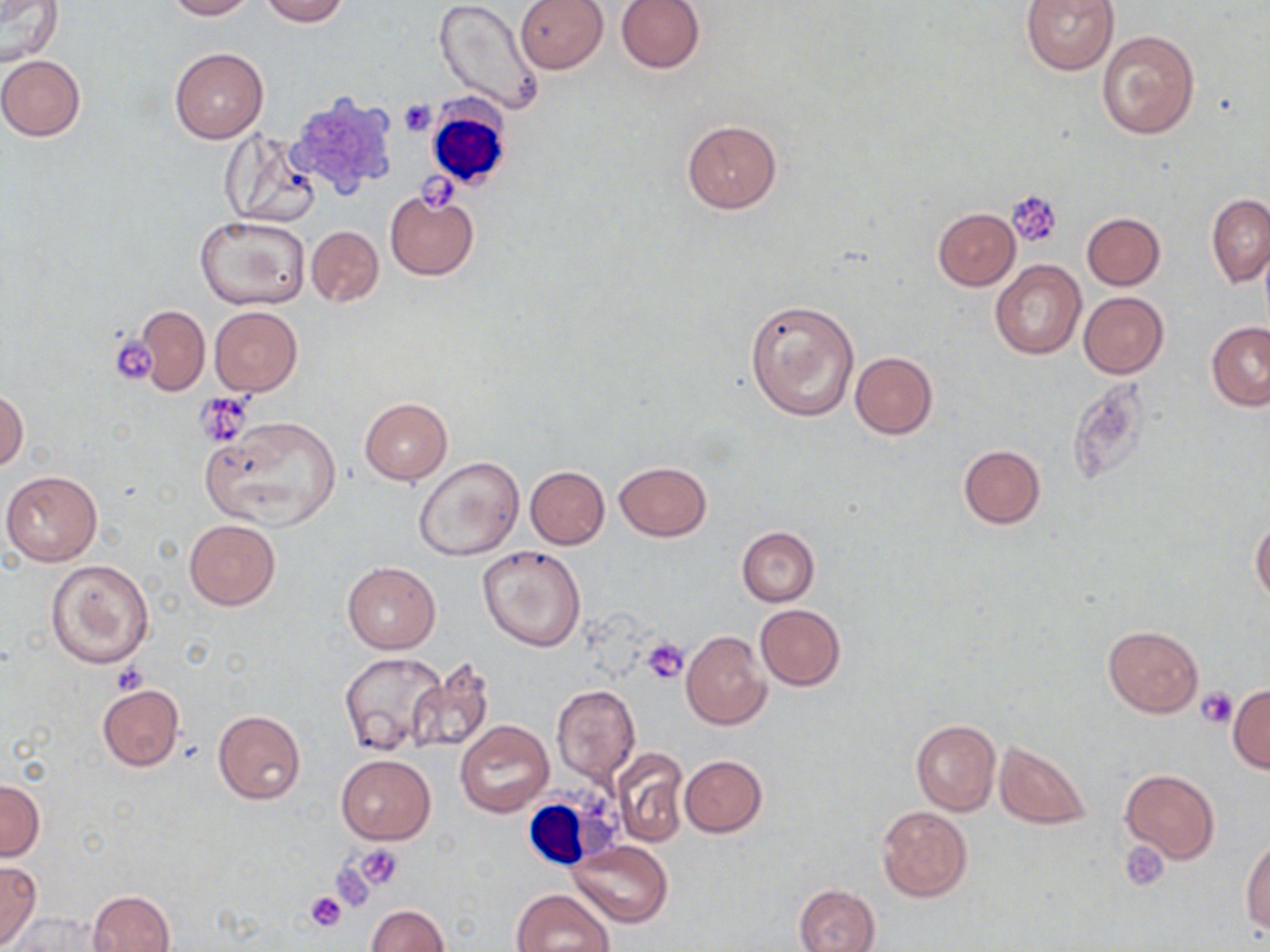

Summary:
  - Coordinate format: approximate bounding boxes as (x1,y1)-(x2,y2) corner pairs in pixels
  - Platelet locations: (399,99)-(436,136), (1008,191)-(1064,249), (108,332)-(159,386), (196,394)-(252,445), (642,637)-(688,684), (110,663)-(149,696), (1197,688)-(1237,729), (1120,841)-(1171,892), (354,843)-(404,891), (331,861)-(376,911), (306,891)-(347,931)
  - White blood cell locations: (423,102)-(513,191), (520,790)-(618,881)
  - Uninfected red blood cell locations: (0,0)-(65,65), (163,0)-(257,20), (259,0)-(348,26), (433,0)-(542,116), (514,0)-(607,74), (616,0)-(706,74), (1021,0)-(1118,74), (1096,29)-(1200,140), (169,48)-(268,143), (0,55)-(85,140), (682,119)-(782,215), (221,133)-(321,228), (384,189)-(478,280), (1206,193)-(1270,287), (932,208)-(1020,290), (1082,212)-(1164,289), (195,214)-(309,311), (306,225)-(382,307), (989,260)-(1086,359), (1078,292)-(1169,378), (745,298)-(860,422), (134,305)-(209,395), (209,306)-(302,397), (1206,322)-(1270,410), (850,351)-(937,438), (1,387)-(28,473), (359,397)-(453,484), (200,417)-(342,531), (956,445)-(1047,529), (414,457)-(524,563), (614,461)-(711,541), (525,466)-(610,549), (2,470)-(102,566), (1251,517)-(1270,604), (184,519)-(280,610), (737,527)-(820,606), (478,545)-(586,651), (46,559)-(154,668), (342,560)-(441,654), (754,604)-(845,690), (1103,625)-(1203,717), (681,631)-(770,729), (340,651)-(446,758), (406,657)-(495,754), (96,684)-(184,771), (551,685)-(640,785), (1227,685)-(1270,773), (212,710)-(306,804), (911,717)-(1001,816), (455,719)-(553,817), (993,739)-(1093,830), (611,748)-(688,847), (336,754)-(436,844), (679,755)-(767,836), (1119,768)-(1220,864), (0,779)-(45,860), (876,806)-(972,902), (1242,838)-(1270,933), (569,840)-(672,927), (0,862)-(42,949), (794,883)-(880,952), (513,888)-(614,952), (88,890)-(175,951), (365,904)-(449,952), (15,913)-(106,951)
  - Slide-level diagnosis: no evidence of blood parasites
  - Modality: light microscopy
  - Image size: 1270×952 pixels
  - Preparation: thin blood smear
  - Field of view: one of a larger specimen
  - Magnification: 1000x
  - Stain: May-Grünwald-Giemsa